Classify this cell by malaria status.
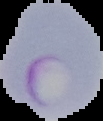

Parasitized.

image type = cell region segmented out of the field of view; surrounding area masked to black
preparation = thin blood smear
image size = 103×121 pixels